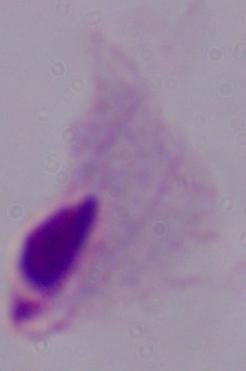

A trichomonad is seen. Photomicrograph. 1000x magnification.